Assess this cell for malaria.
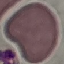
It is uninfected.

Acquired by smartphone through the microscope eyepiece. Thin blood smear. Automatically extracted cell patch, resized to 64 × 64 pixels. Giemsa stain.